Assess this cell for malaria.
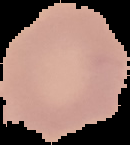
Uninfected.

Summary:
  - Image type: cell region segmented out of the field of view; surrounding area masked to black
  - Image size: 130×145 pixels
  - Preparation: thin blood smear